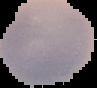

image type = cell region segmented out of the field of view; surrounding area masked to black
preparation = thin blood film
result = negative for malaria parasites
image size = 97×88 pixels